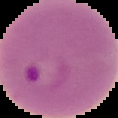
From a thin blood film. Image is 118×118 pixels. Malaria status: parasitized. Cell region segmented out of the field of view; the surrounding area is masked to black.